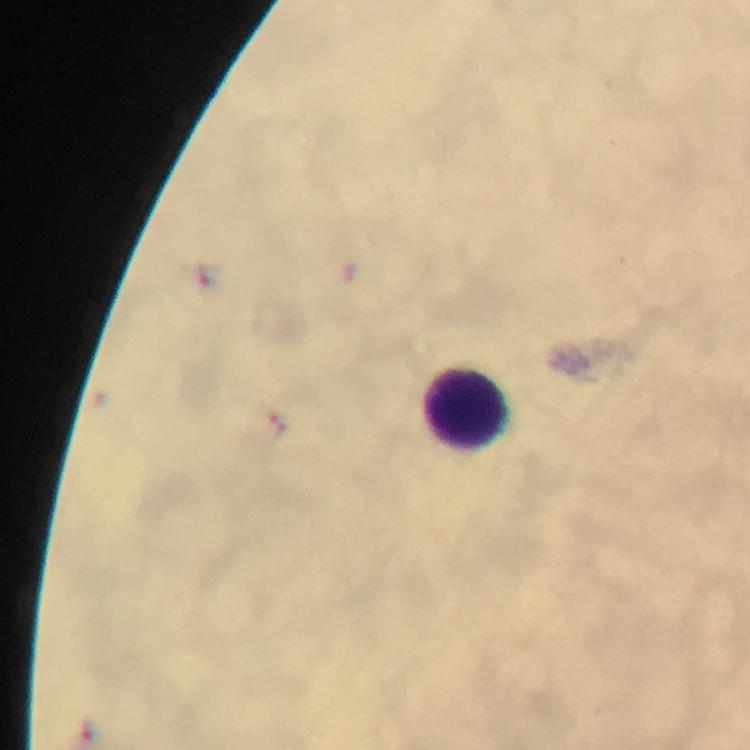
{
  "cropped_from": "a single field of view",
  "image_size": "750×750 pixels",
  "magnification": "100x",
  "context": "from a malaria diagnostic workup",
  "leukocyte_locations": "approximate centers as (x, y) in pixels: (466, 410)",
  "immersion_oil": "used",
  "stain": "Giemsa",
  "preparation": "thick smear",
  "capture": "smartphone camera through the microscope",
  "plasmodium_parasites": "none seen"
}